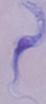

Photomicrograph. A trypanosome is seen. Captured at 1000x magnification.